Assess the morphology of the erythrocytes.
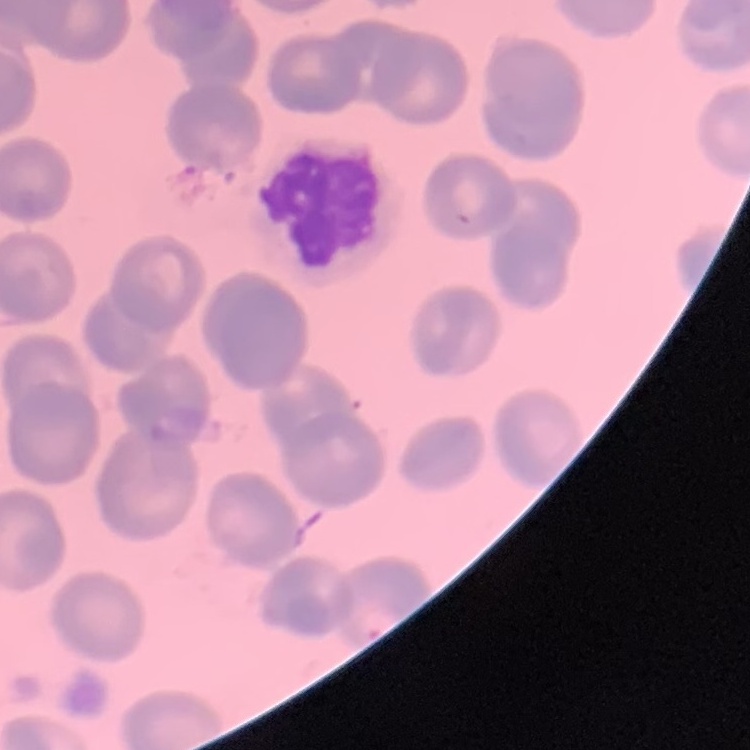
No rouleaux formation.

Stained with either Field's or Giemsa. Thin peripheral smear. One tile cut from a larger photomicrograph.